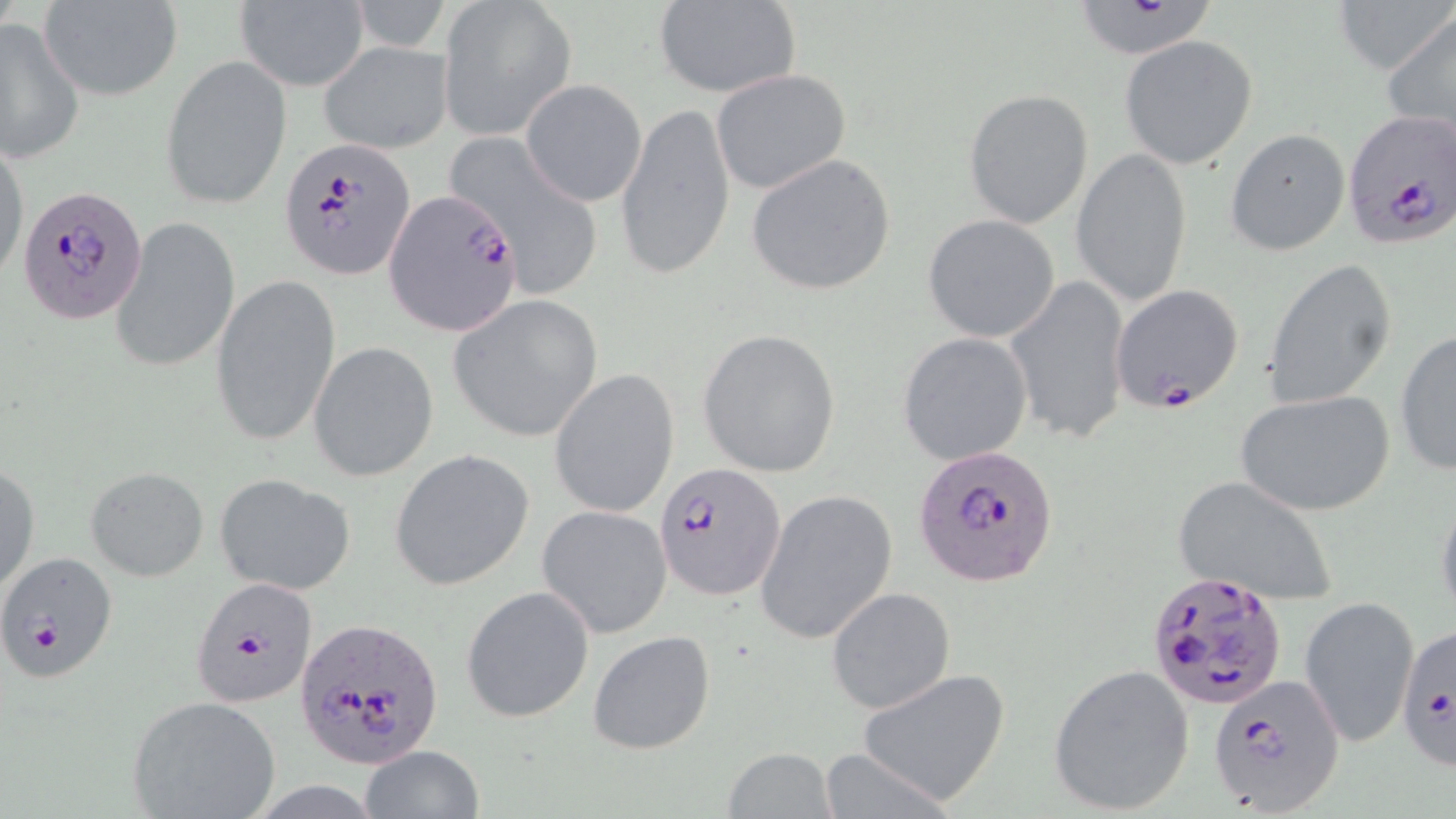 Approximate bounding boxes as named x1/y1/x2/y2 corners in pixels. Plasmodium falciparum-infected red blood cell locations: (x1=1340, y1=111, x2=1456, y2=250), (x1=281, y1=138, x2=414, y2=279), (x1=17, y1=186, x2=148, y2=325), (x1=384, y1=188, x2=523, y2=334), (x1=1109, y1=283, x2=1244, y2=413), (x1=915, y1=442, x2=1058, y2=587), (x1=655, y1=464, x2=784, y2=598), (x1=0, y1=552, x2=119, y2=684), (x1=1147, y1=569, x2=1287, y2=709), (x1=189, y1=576, x2=319, y2=708), (x1=292, y1=615, x2=445, y2=769), (x1=1397, y1=623, x2=1456, y2=773), (x1=1208, y1=673, x2=1344, y2=816). Uninfected red blood cell locations: (x1=438, y1=0, x2=577, y2=139), (x1=1333, y1=0, x2=1450, y2=76), (x1=234, y1=1, x2=369, y2=92), (x1=41, y1=2, x2=179, y2=100), (x1=351, y1=2, x2=452, y2=53), (x1=652, y1=2, x2=801, y2=97), (x1=1073, y1=3, x2=1219, y2=60), (x1=1382, y1=11, x2=1456, y2=146), (x1=0, y1=18, x2=85, y2=164), (x1=1120, y1=36, x2=1258, y2=169), (x1=320, y1=41, x2=453, y2=155), (x1=160, y1=54, x2=292, y2=212), (x1=712, y1=69, x2=850, y2=195), (x1=522, y1=79, x2=646, y2=207), (x1=963, y1=89, x2=1094, y2=228), (x1=617, y1=100, x2=737, y2=284), (x1=1226, y1=129, x2=1350, y2=254), (x1=445, y1=133, x2=605, y2=298), (x1=1, y1=139, x2=28, y2=286), (x1=1071, y1=148, x2=1193, y2=309), (x1=745, y1=153, x2=897, y2=296), (x1=923, y1=215, x2=1060, y2=342), (x1=110, y1=216, x2=239, y2=374), (x1=1264, y1=257, x2=1397, y2=410), (x1=1004, y1=276, x2=1132, y2=441), (x1=211, y1=277, x2=340, y2=450), (x1=447, y1=295, x2=604, y2=443), (x1=696, y1=328, x2=843, y2=477), (x1=1394, y1=329, x2=1456, y2=476), (x1=898, y1=332, x2=1034, y2=467), (x1=307, y1=341, x2=440, y2=481), (x1=548, y1=367, x2=679, y2=519), (x1=1238, y1=388, x2=1396, y2=516), (x1=391, y1=450, x2=536, y2=592), (x1=1, y1=461, x2=39, y2=595), (x1=85, y1=466, x2=209, y2=582), (x1=213, y1=474, x2=356, y2=596), (x1=1173, y1=475, x2=1340, y2=607), (x1=754, y1=488, x2=897, y2=645), (x1=1434, y1=488, x2=1456, y2=624), (x1=538, y1=505, x2=673, y2=639), (x1=462, y1=585, x2=596, y2=725), (x1=826, y1=587, x2=956, y2=716), (x1=1300, y1=596, x2=1419, y2=746), (x1=588, y1=630, x2=715, y2=756), (x1=1046, y1=665, x2=1195, y2=815), (x1=855, y1=668, x2=1011, y2=806), (x1=126, y1=695, x2=281, y2=818), (x1=360, y1=745, x2=484, y2=819), (x1=817, y1=746, x2=958, y2=818), (x1=721, y1=748, x2=837, y2=819). Slide-level diagnosis: Plasmodium falciparum. Captured at 1000x magnification. Light microscopy. May-Grünwald-Giemsa stain. Single field of view. Thin blood film. Image is 1456×819 pixels.